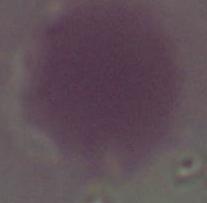
Summary:
  - Magnification: 1000x
  - Modality: micrograph
  - Identification: erythrocyte